Outline each Plasmodium falciparum-infected red blood cell.
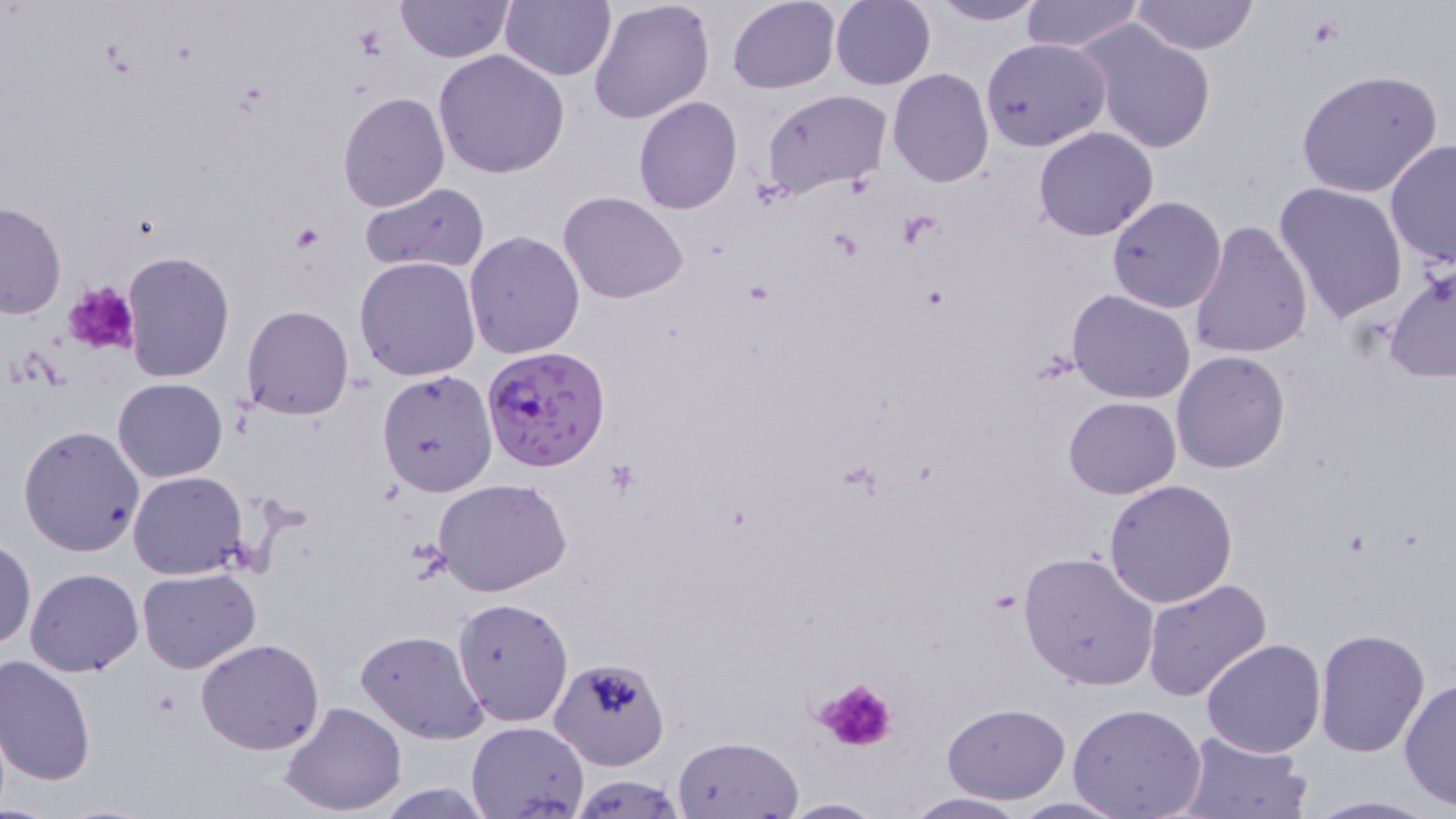
Approximate bounding boxes as (x1, y1, x2, y2) in pixels.
Plasmodium falciparum-infected red blood cells: (481, 344, 611, 474).

slide-level diagnosis = Plasmodium falciparum
stain = May-Grünwald-Giemsa
field of view = single
modality = optical microscopy
preparation = thin blood smear
image size = 1456×819 pixels
platelet locations = approximate bounding boxes as (x1, y1, x2, y2) in pixels: (354, 25, 387, 59), (289, 225, 323, 253), (62, 281, 142, 357), (810, 674, 902, 756)
uninfected red blood cell locations = approximate bounding boxes as (x1, y1, x2, y2) in pixels: (395, 0, 511, 62), (500, 0, 615, 81), (587, 0, 714, 124), (726, 0, 840, 92), (830, 0, 936, 90), (1019, 0, 1144, 52), (1129, 0, 1260, 55), (925, 1, 1052, 26), (1080, 21, 1216, 154), (980, 36, 1109, 152), (434, 49, 569, 178), (887, 69, 995, 187), (1294, 69, 1444, 198), (761, 88, 891, 199), (338, 91, 450, 211), (633, 97, 742, 215), (1033, 127, 1159, 242), (1385, 139, 1456, 270), (1274, 182, 1408, 324), (360, 183, 490, 275), (558, 191, 688, 305), (1107, 196, 1227, 314), (1, 200, 67, 318), (1187, 219, 1312, 361), (462, 231, 585, 358), (121, 250, 234, 381), (354, 256, 482, 382), (1384, 261, 1455, 383), (1067, 289, 1197, 405), (240, 304, 356, 419), (1171, 351, 1290, 474), (376, 370, 497, 497), (113, 377, 227, 482), (1064, 396, 1181, 498), (18, 425, 146, 558), (128, 470, 248, 580), (432, 479, 573, 598), (1103, 479, 1240, 610), (0, 541, 36, 650), (1019, 550, 1162, 691), (24, 568, 142, 677), (138, 569, 260, 673), (1142, 578, 1273, 704), (451, 598, 573, 726), (357, 629, 490, 744), (1312, 629, 1432, 757), (1201, 637, 1327, 757), (195, 638, 325, 756), (547, 655, 669, 771), (0, 656, 96, 788), (1400, 678, 1456, 809), (281, 701, 408, 817), (940, 701, 1071, 803), (1066, 702, 1209, 819), (467, 721, 589, 818), (1171, 729, 1313, 818), (673, 734, 803, 819), (568, 774, 688, 817), (368, 781, 500, 818), (898, 792, 1033, 818), (1297, 794, 1447, 818), (779, 796, 884, 817), (1006, 796, 1132, 817)
magnification = 1000x